Report the malaria status of this cell.
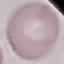

It is uninfected.

Thin blood film. Giemsa stain. Acquired by smartphone through the microscope eyepiece. Automatically extracted cell patch, resized to 64 × 64 pixels.